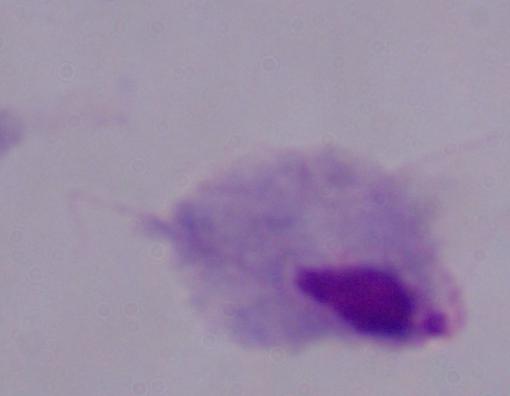

identification = trichomonad
magnification = 1000x
modality = micrograph